Report the malaria status of this cell.
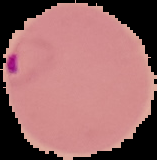
Parasitized.

From a thin blood smear. Cell region segmented out of the field of view; the surrounding area is masked to black. Image is 157×160 pixels.